Look for Plasmodium parasites.
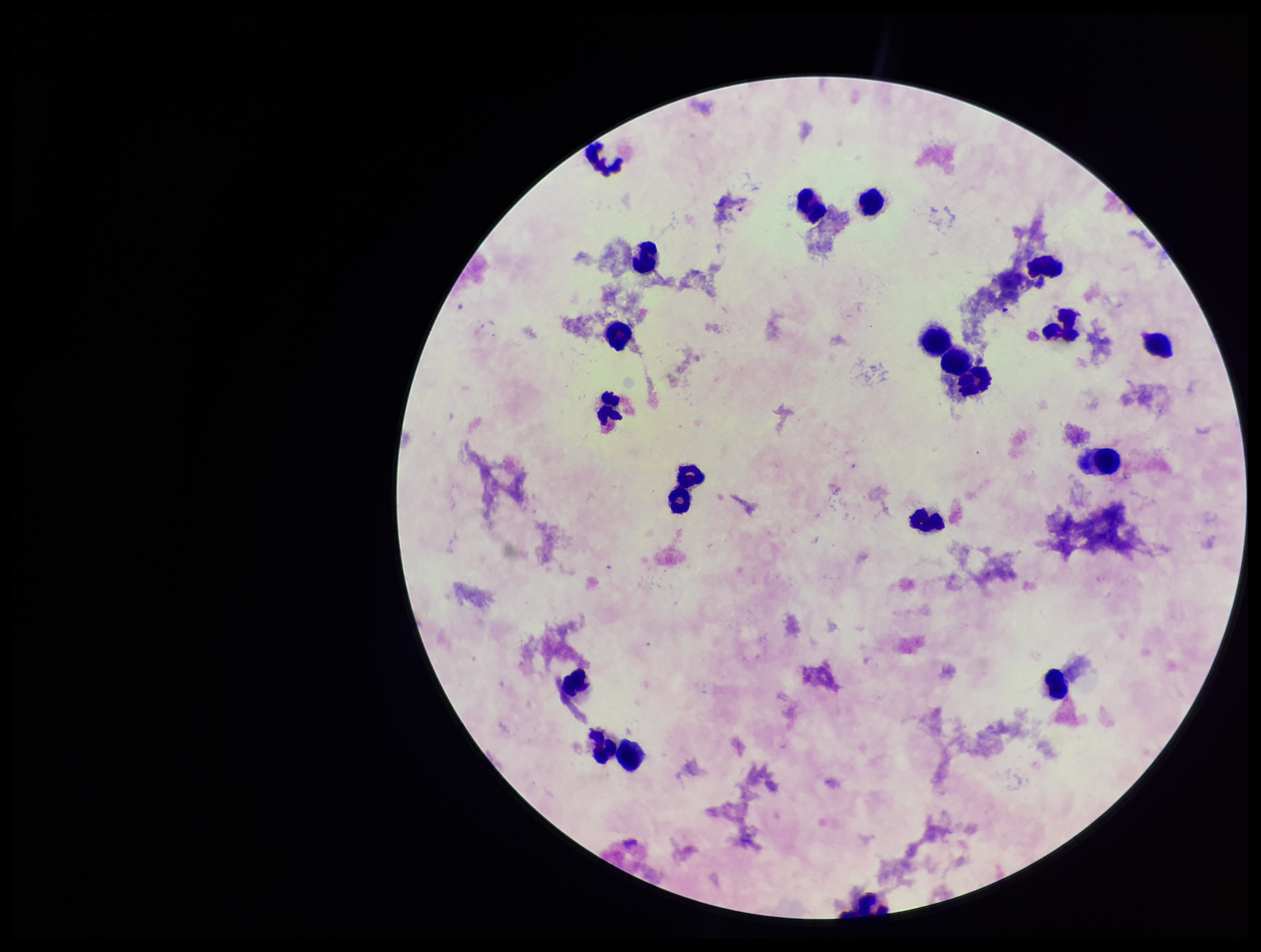

None seen.

Giemsa stain. Parasite count: 0. Single field of view. Preparation: thick smear. Photographed through the microscope eyepiece with a smartphone camera. Patient malaria status: infected. Species reported for this patient: Plasmodium vivax. Image is 1261×952 pixels. Leukocyte count: 20.